Name the cell type shown.
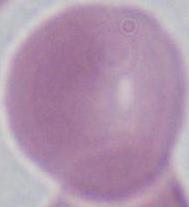
An erythrocyte.

Summary:
  - Modality: photomicrograph
  - Magnification: 1000x